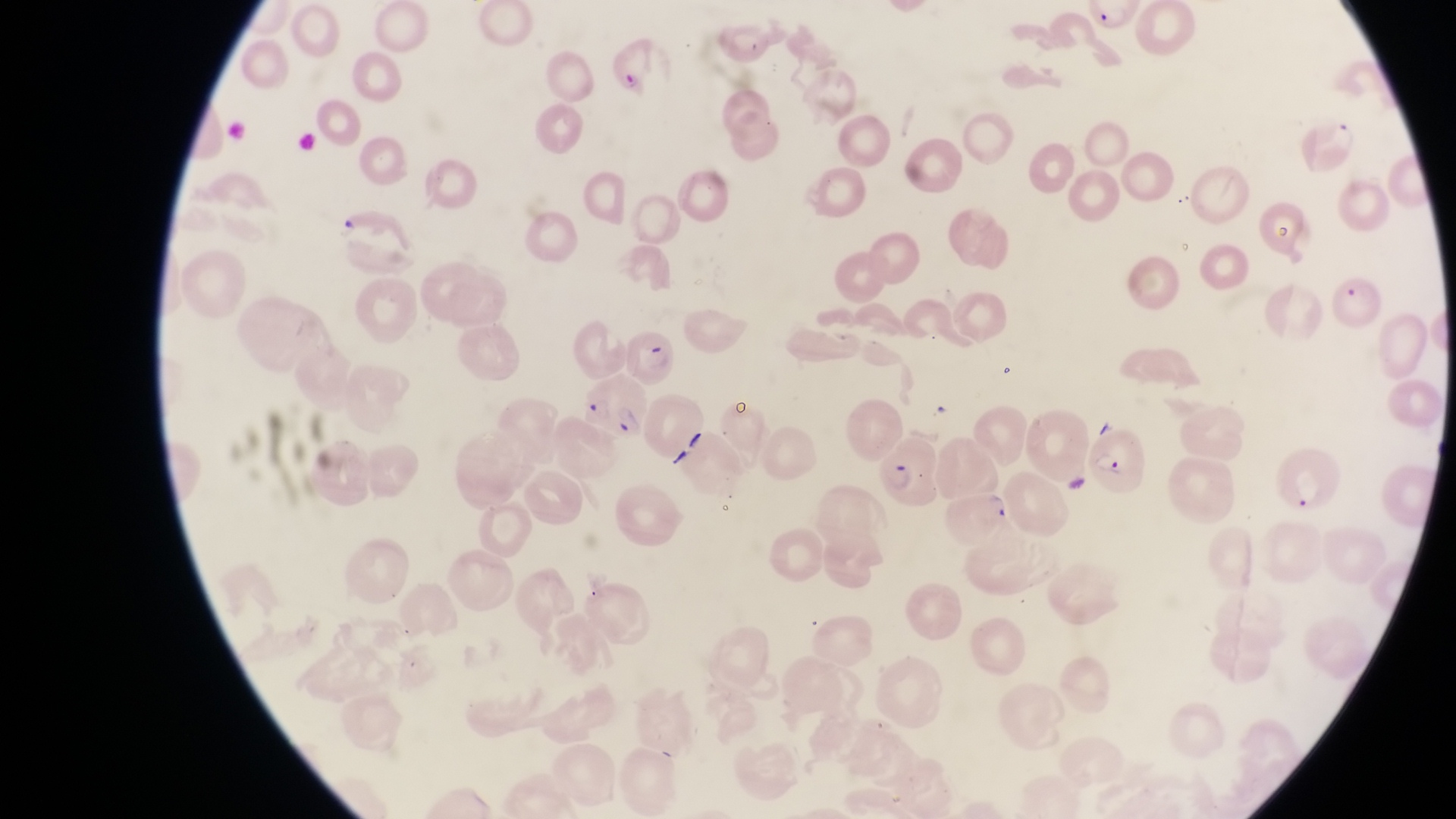

{
  "artifact_platelet_like_body_stain_precipitate_or_debris_locations": "approximate bounding boxes as left top right bottom in pixels: 337 211 364 240",
  "image_size": "1456×819 pixels",
  "capture": "smartphone photograph through the eyepiece of an Olympus CX-23 microscope",
  "magnification": "1000x",
  "field_of_view": "single",
  "parasitised_red_blood_cell_locations": "approximate bounding boxes as left top right bottom in pixels: 704 21 765 70; 607 36 678 102; 1297 105 1358 178; 620 328 678 388; 582 375 648 441; 875 426 941 509; 1093 431 1146 491; 946 492 1015 544",
  "country": "Uganda",
  "preparation": "thin blood film"
}